Report the malaria status of this cell.
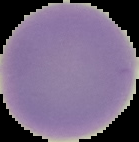
It is uninfected.

Summary:
  - Preparation: thin blood film
  - Image size: 139×142 pixels
  - Image type: cell region segmented out of the field of view; surrounding area masked to black